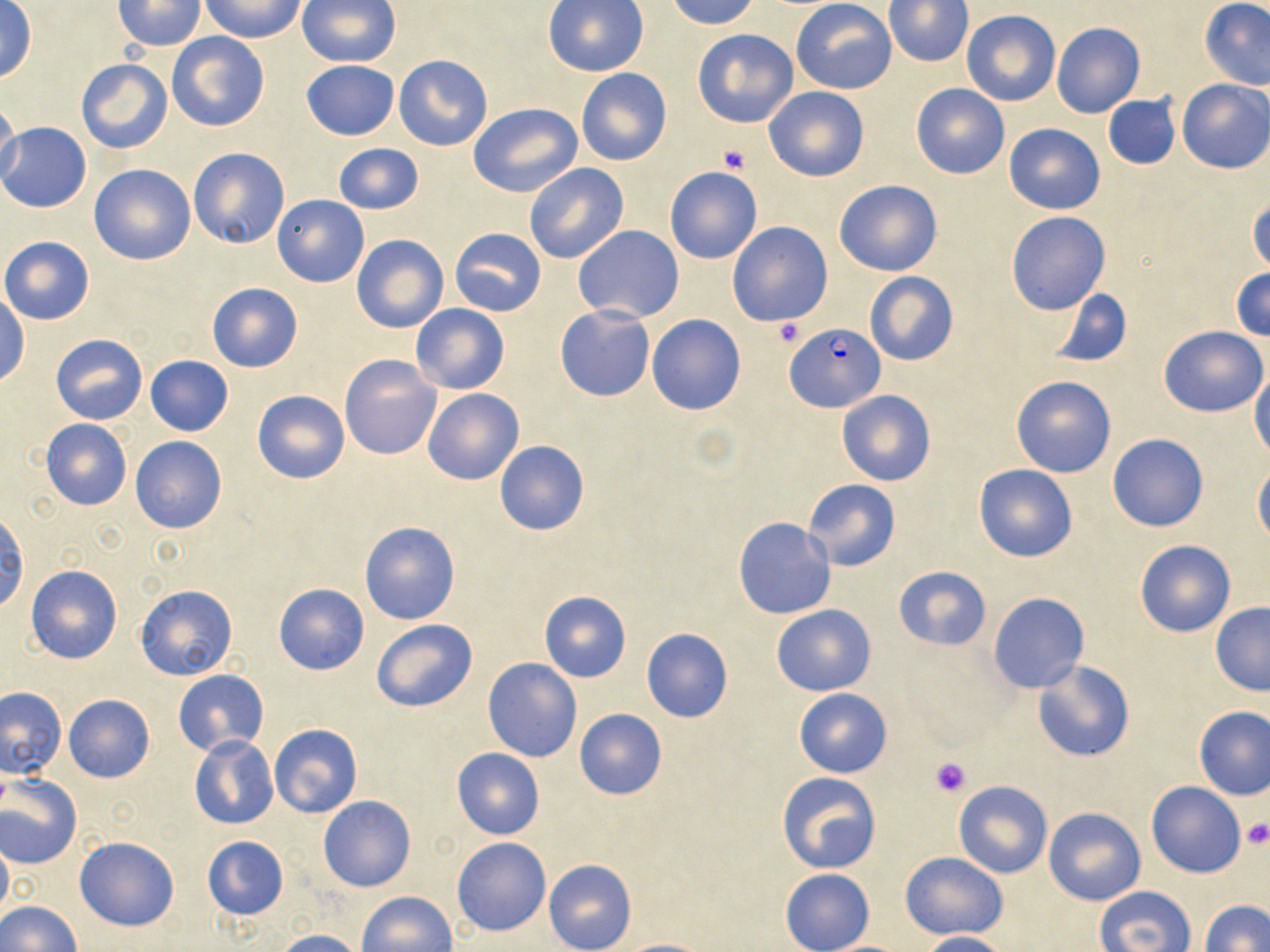

Summary:
  - Coordinate format: approximate bounding boxes as named x1/y1/x2/y2 corners in pixels
  - Plasmodium falciparum-infected red blood cell locations: (x1=787, y1=322, x2=885, y2=414)
  - Uninfected red blood cell locations: (x1=201, y1=0, x2=306, y2=42), (x1=664, y1=0, x2=760, y2=29), (x1=791, y1=0, x2=897, y2=94), (x1=114, y1=1, x2=206, y2=51), (x1=296, y1=1, x2=400, y2=68), (x1=542, y1=1, x2=649, y2=76), (x1=885, y1=1, x2=972, y2=67), (x1=1200, y1=1, x2=1270, y2=88), (x1=0, y1=2, x2=38, y2=83), (x1=960, y1=10, x2=1060, y2=106), (x1=1051, y1=21, x2=1146, y2=119), (x1=693, y1=28, x2=798, y2=128), (x1=167, y1=32, x2=270, y2=132), (x1=393, y1=53, x2=494, y2=152), (x1=75, y1=59, x2=172, y2=154), (x1=301, y1=59, x2=400, y2=140), (x1=575, y1=68, x2=672, y2=166), (x1=1176, y1=80, x2=1270, y2=173), (x1=910, y1=82, x2=1010, y2=179), (x1=764, y1=86, x2=870, y2=182), (x1=1103, y1=94, x2=1179, y2=171), (x1=0, y1=98, x2=21, y2=190), (x1=469, y1=103, x2=583, y2=198), (x1=0, y1=122, x2=91, y2=213), (x1=1005, y1=122, x2=1104, y2=214), (x1=331, y1=144, x2=424, y2=215), (x1=188, y1=147, x2=291, y2=249), (x1=524, y1=163, x2=629, y2=264), (x1=89, y1=164, x2=197, y2=266), (x1=664, y1=167, x2=764, y2=265), (x1=834, y1=178, x2=943, y2=276), (x1=272, y1=195, x2=369, y2=287), (x1=1247, y1=195, x2=1270, y2=277), (x1=1006, y1=211, x2=1110, y2=315), (x1=727, y1=222, x2=833, y2=327), (x1=573, y1=225, x2=684, y2=323), (x1=450, y1=228, x2=545, y2=317), (x1=351, y1=234, x2=449, y2=333), (x1=0, y1=237, x2=94, y2=325), (x1=1232, y1=267, x2=1270, y2=343), (x1=863, y1=272, x2=959, y2=366), (x1=206, y1=282, x2=304, y2=373), (x1=1049, y1=288, x2=1134, y2=369), (x1=0, y1=294, x2=29, y2=386), (x1=410, y1=304, x2=510, y2=394), (x1=554, y1=305, x2=655, y2=402), (x1=646, y1=314, x2=745, y2=416), (x1=1160, y1=326, x2=1268, y2=417), (x1=51, y1=334, x2=148, y2=425), (x1=145, y1=355, x2=233, y2=436), (x1=340, y1=356, x2=441, y2=460), (x1=1249, y1=365, x2=1270, y2=461), (x1=1012, y1=375, x2=1116, y2=478), (x1=422, y1=389, x2=524, y2=486), (x1=252, y1=390, x2=351, y2=484), (x1=836, y1=390, x2=934, y2=486), (x1=40, y1=419, x2=131, y2=511), (x1=1107, y1=433, x2=1209, y2=532), (x1=130, y1=436, x2=228, y2=535), (x1=494, y1=440, x2=590, y2=536), (x1=1253, y1=462, x2=1270, y2=545), (x1=972, y1=463, x2=1078, y2=562), (x1=802, y1=479, x2=900, y2=571), (x1=0, y1=510, x2=28, y2=614), (x1=732, y1=517, x2=836, y2=619), (x1=359, y1=520, x2=462, y2=626), (x1=1134, y1=540, x2=1236, y2=637), (x1=26, y1=564, x2=122, y2=663), (x1=892, y1=566, x2=991, y2=649), (x1=273, y1=583, x2=369, y2=675), (x1=134, y1=585, x2=238, y2=681), (x1=539, y1=591, x2=631, y2=682), (x1=988, y1=592, x2=1089, y2=694), (x1=1210, y1=603, x2=1270, y2=696), (x1=771, y1=604, x2=876, y2=696), (x1=371, y1=619, x2=477, y2=713), (x1=640, y1=628, x2=734, y2=723), (x1=483, y1=658, x2=582, y2=762), (x1=1031, y1=659, x2=1135, y2=763), (x1=173, y1=669, x2=268, y2=756), (x1=0, y1=685, x2=66, y2=779), (x1=794, y1=688, x2=892, y2=777), (x1=63, y1=695, x2=155, y2=783), (x1=1193, y1=706, x2=1269, y2=800), (x1=573, y1=708, x2=668, y2=800), (x1=269, y1=723, x2=363, y2=819), (x1=189, y1=735, x2=278, y2=831), (x1=450, y1=748, x2=545, y2=839), (x1=776, y1=772, x2=881, y2=874), (x1=0, y1=775, x2=82, y2=869), (x1=953, y1=781, x2=1052, y2=878), (x1=1146, y1=781, x2=1246, y2=878), (x1=318, y1=796, x2=417, y2=892), (x1=1044, y1=807, x2=1145, y2=905), (x1=202, y1=835, x2=288, y2=922), (x1=0, y1=836, x2=12, y2=922), (x1=452, y1=836, x2=551, y2=936), (x1=75, y1=837, x2=180, y2=931), (x1=900, y1=850, x2=1008, y2=940), (x1=544, y1=859, x2=636, y2=952), (x1=780, y1=868, x2=874, y2=952), (x1=1094, y1=887, x2=1195, y2=952), (x1=357, y1=891, x2=457, y2=952), (x1=0, y1=900, x2=80, y2=951), (x1=1201, y1=900, x2=1270, y2=952), (x1=273, y1=929, x2=364, y2=952), (x1=914, y1=931, x2=1010, y2=951), (x1=614, y1=938, x2=713, y2=952)
  - Platelet locations: (x1=717, y1=145, x2=750, y2=175), (x1=772, y1=319, x2=805, y2=346), (x1=929, y1=755, x2=972, y2=797), (x1=1241, y1=820, x2=1270, y2=849)
  - Slide-level diagnosis: Plasmodium falciparum
  - Field of view: one of a larger specimen
  - Modality: light microscopy
  - Image size: 1270×952 pixels
  - Magnification: 1000x
  - Preparation: thin blood smear
  - Stain: May-Grünwald-Giemsa